Look for Plasmodium parasites.
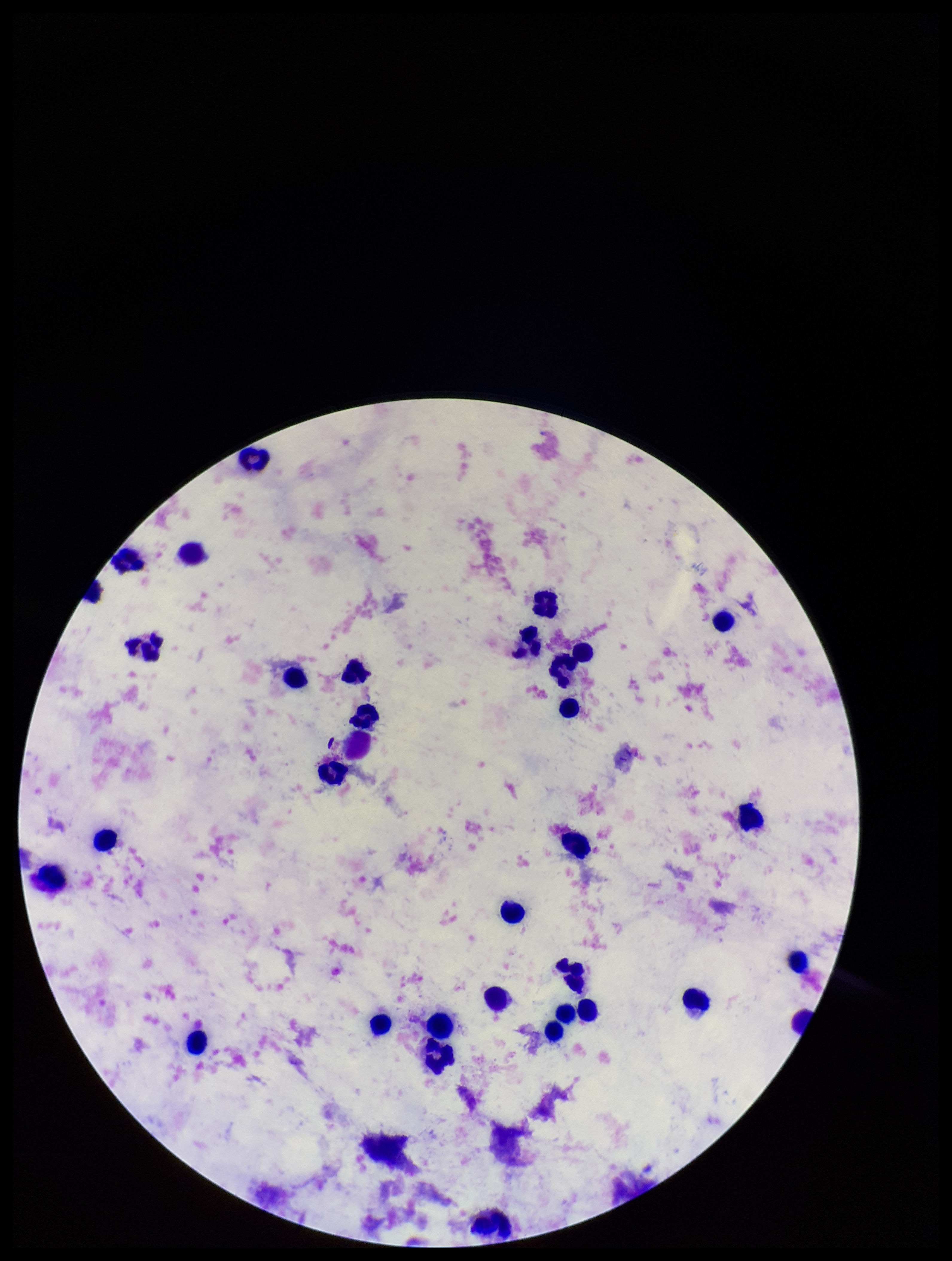

None identified.

Summary:
  - Parasite count: 0
  - Leukocyte count: 34
  - Capture: smartphone photograph through the microscope eyepiece
  - Stain: Giemsa
  - Image size: 952×1261 pixels
  - Field of view: single
  - Preparation: thick smear
  - Patient malaria status: negative